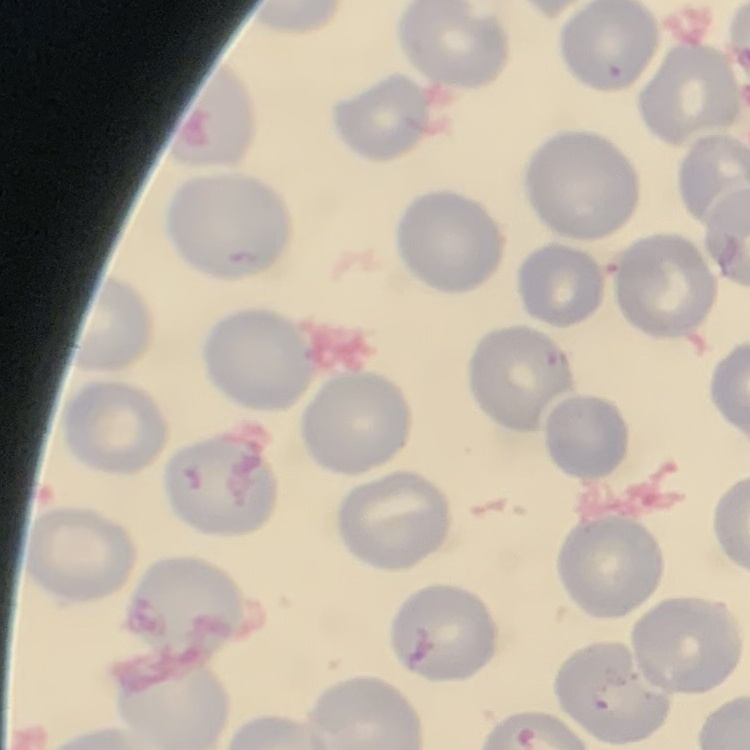

red blood cell morphology = no rouleaux formation
stain = Field's or Giemsa
preparation = thin blood film
image type = square crop of a larger photomicrograph